Name the cell type shown.
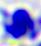

A leukocyte.

Summary:
  - Magnification: 400x
  - Modality: photomicrograph